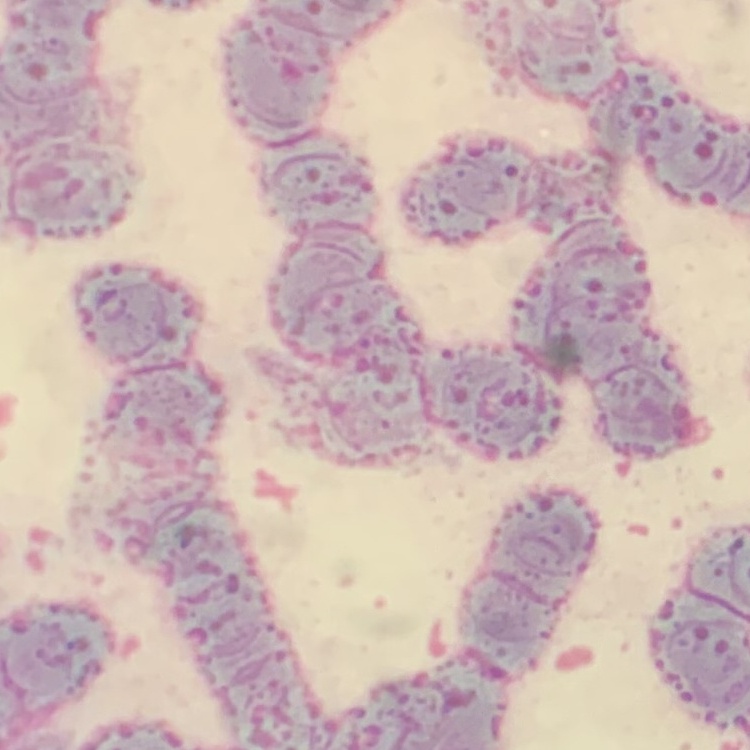
erythrocyte morphology = rouleaux formation
image type = square crop of a larger photomicrograph
stain = Field's or Giemsa
preparation = thin blood film